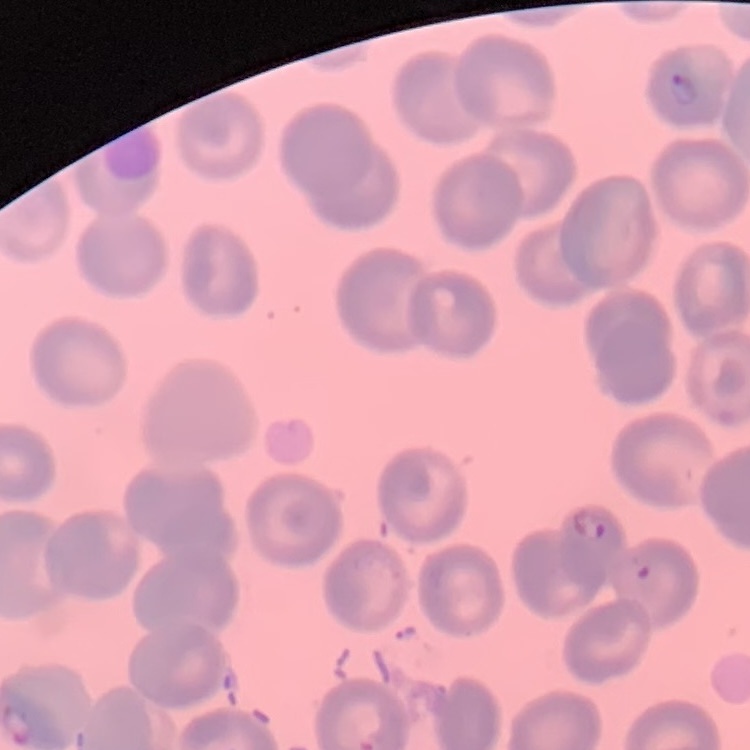 The erythrocytes show no rouleaux formation. Thin peripheral smear. Stained with either Field's or Giemsa. One tile cut from a larger photomicrograph.